Locate every blood parasite and identify its species.
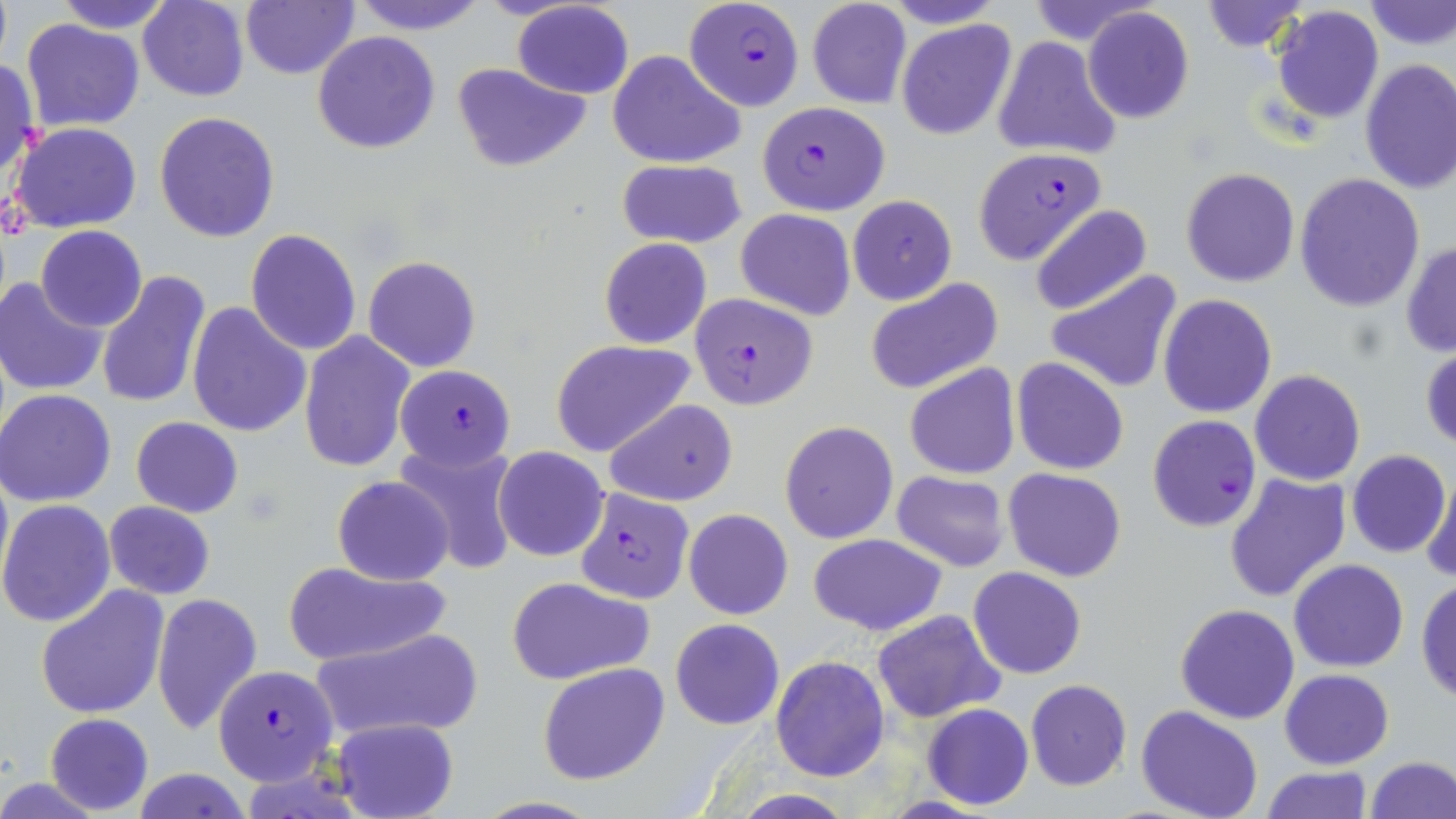
Approximate bounding boxes as (x1, y1, x2, y2) in pixels.
Plasmodium falciparum-infected red blood cells: (683, 0, 805, 109), (759, 102, 888, 213), (972, 147, 1102, 265), (689, 292, 818, 409), (394, 365, 515, 468), (1147, 415, 1261, 532), (574, 486, 695, 604), (212, 663, 339, 785).
No Plasmodium ovale, Plasmodium malariae, Plasmodium vivax, Babesia divergens, or Trypanosoma brucei observed.

Uninfected red blood cell locations: (0, 0, 12, 68), (52, 0, 178, 33), (348, 0, 491, 35), (510, 0, 635, 99), (805, 0, 912, 109), (883, 0, 1007, 28), (1197, 0, 1312, 53), (1361, 0, 1456, 51), (137, 1, 250, 102), (240, 1, 359, 79), (1270, 5, 1385, 125), (1081, 7, 1195, 122), (22, 18, 144, 129), (896, 19, 1017, 140), (312, 30, 441, 154), (992, 35, 1121, 163), (610, 51, 745, 167), (0, 57, 41, 182), (1359, 58, 1456, 194), (451, 61, 591, 172), (154, 111, 280, 243), (10, 122, 143, 233), (616, 159, 747, 249), (1180, 167, 1300, 288), (1295, 174, 1425, 312), (846, 195, 957, 305), (1029, 204, 1153, 317), (736, 209, 856, 319), (36, 225, 147, 331), (245, 228, 362, 355), (599, 238, 711, 349), (1401, 239, 1456, 359), (363, 255, 481, 373), (1046, 268, 1185, 394), (96, 269, 213, 413), (0, 277, 108, 395), (865, 278, 1004, 396), (1157, 294, 1278, 419), (186, 301, 312, 439), (298, 331, 415, 472), (552, 339, 695, 457), (1421, 344, 1455, 452), (1012, 358, 1128, 474), (904, 364, 1019, 479), (1249, 369, 1365, 486), (0, 389, 116, 507), (605, 398, 739, 505), (131, 417, 242, 517), (780, 419, 898, 545), (395, 441, 520, 576), (493, 446, 610, 561), (1346, 450, 1451, 559), (0, 461, 11, 595), (1003, 467, 1127, 582), (891, 471, 1010, 572), (1422, 471, 1456, 585), (1223, 473, 1351, 605), (332, 476, 454, 586), (0, 498, 118, 627), (103, 501, 215, 600), (684, 509, 792, 619), (807, 533, 948, 637), (1288, 559, 1409, 672), (281, 560, 450, 667), (968, 567, 1087, 678), (505, 576, 656, 686), (1416, 576, 1456, 703), (36, 584, 171, 720), (151, 592, 263, 735), (1175, 604, 1301, 724), (871, 609, 1005, 723), (669, 618, 784, 730), (308, 626, 486, 743), (771, 655, 890, 780), (538, 662, 671, 786), (1280, 669, 1393, 768), (1025, 679, 1131, 791), (921, 704, 1035, 810), (1135, 706, 1264, 819), (44, 712, 153, 814), (334, 718, 459, 819), (1365, 755, 1455, 818), (1260, 766, 1371, 819), (128, 769, 254, 819), (0, 777, 111, 817). Slide-level diagnosis: Plasmodium falciparum. Captured at 1000x magnification. Image is 1456×819 pixels. Thin blood film. Single field of view. Optical microscopy. May-Grünwald-Giemsa stain.